Report the malaria status of this cell.
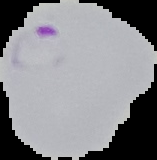

It is parasitized.

Cell region segmented out of the field of view; the surrounding area is masked to black. Image is 157×160 pixels. From a thin blood film.